State which parasite is depicted.
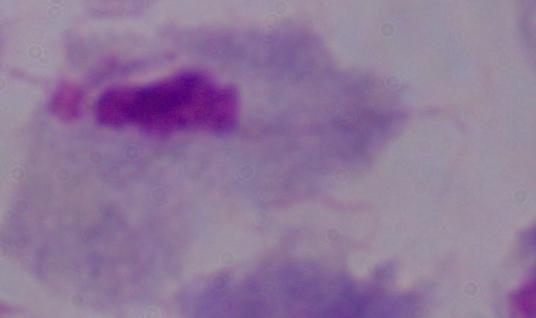
This is a trichomonad.

Captured at 1000x magnification. Photomicrograph.